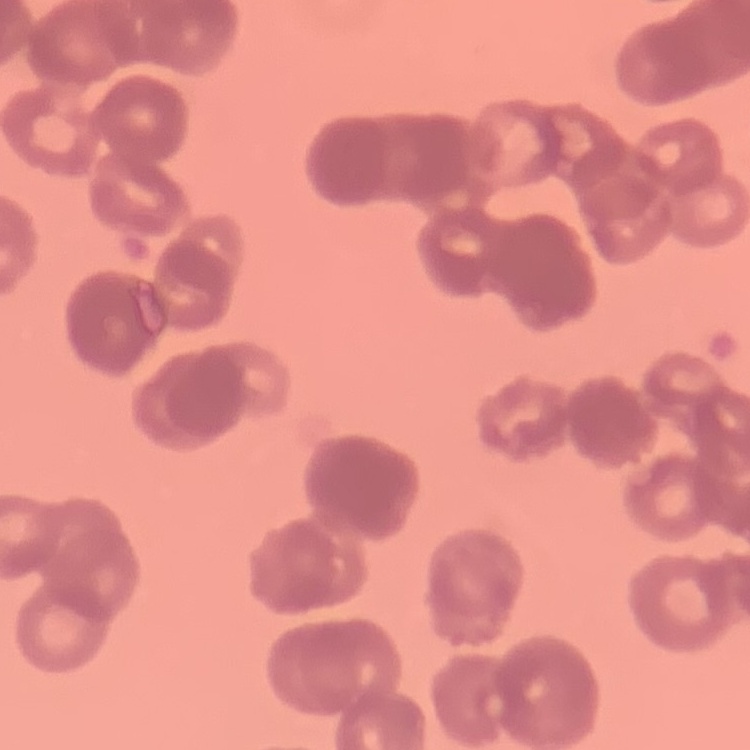
{
  "erythrocyte_morphology": "rouleaux formation",
  "preparation": "thin peripheral smear",
  "image_type": "one tile cut from a larger photomicrograph",
  "stain": "Field's or Giemsa"
}